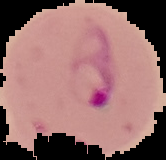
image_size: 166×160 pixels
image_type: segmented cell region on a black background
preparation: thin blood smear
malaria_status: parasitized